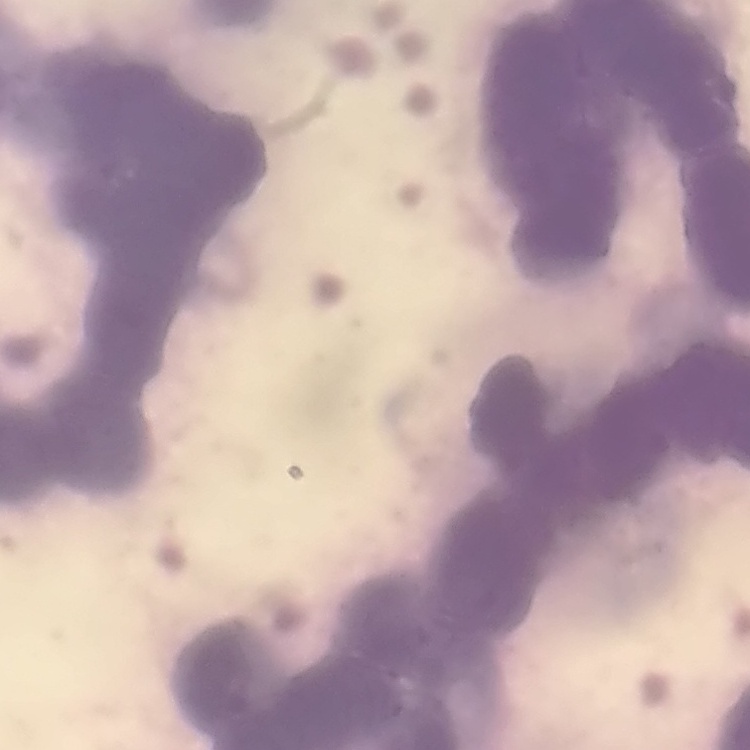

{
  "red_blood_cell_morphology": "rouleaux formation",
  "image_type": "one tile cut from a larger photomicrograph",
  "preparation": "thin blood smear",
  "stain": "Field's or Giemsa"
}